Comment on the morphology of the erythrocytes.
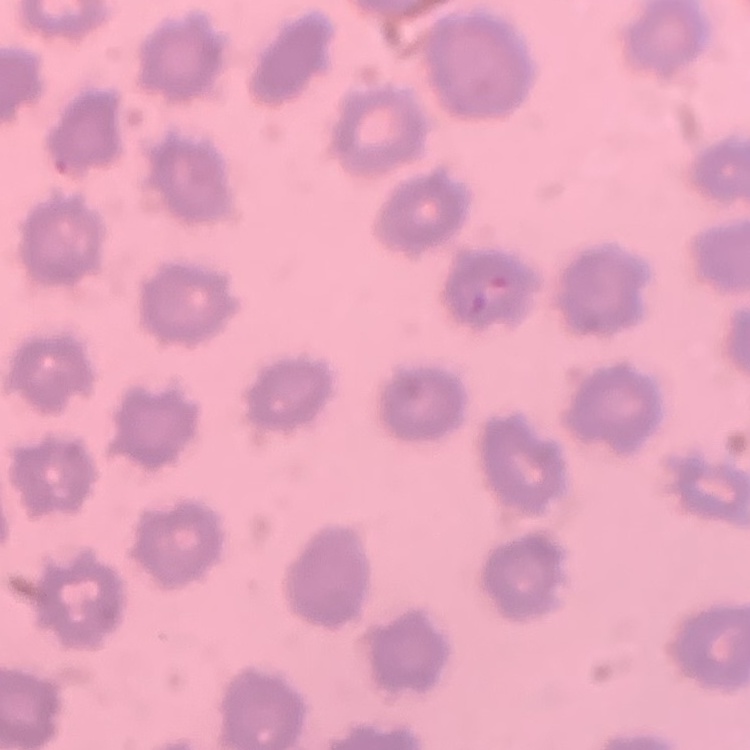
They show no rouleaux formation.

Thin blood film. Stained with either Field's or Giemsa. One tile cut from a larger photomicrograph.